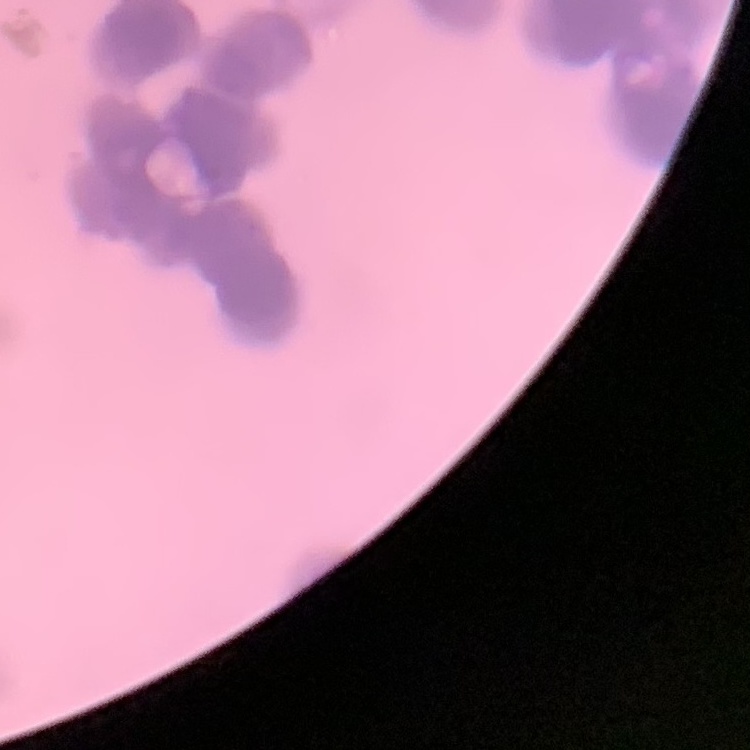

The erythrocytes show rouleaux formation. One tile cut from a larger photomicrograph. Thin blood film. Field's or Giemsa stain.